Report the malaria status of this cell.
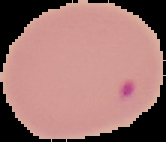

Parasitized.

image type = segmented cell region on a black background
preparation = thin blood smear
image size = 166×142 pixels